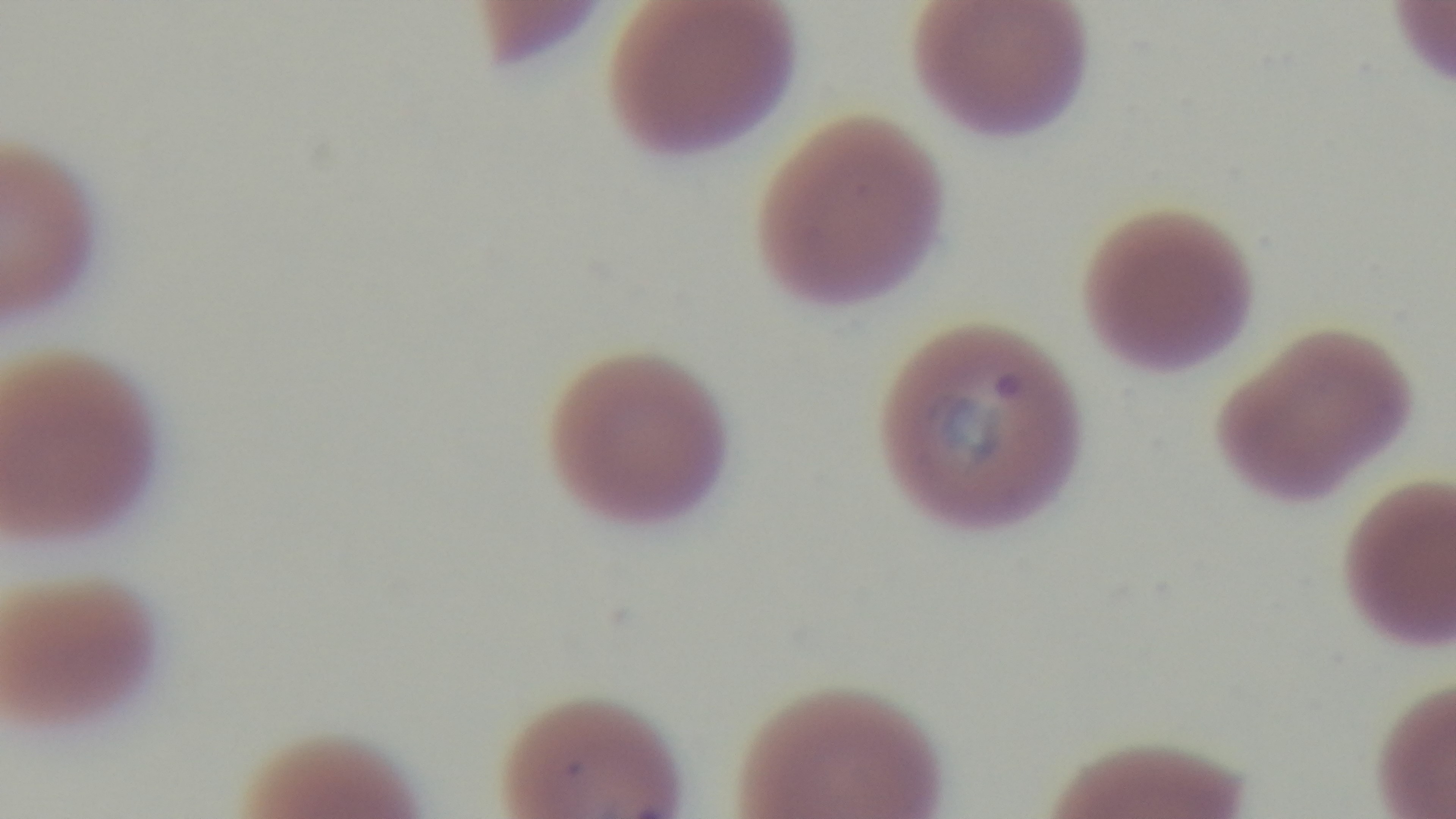
{
  "preparation": "thin blood film",
  "stain": "Giemsa",
  "modality": "light microscopy",
  "field_of_view": "single",
  "objective": "100x oil immersion",
  "capture": "mounted 4K digital camera",
  "malaria_status": "positive"
}